Report the malaria status of this cell.
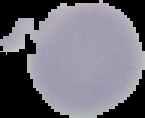

Uninfected.

Summary:
  - Image size: 145×118 pixels
  - Image type: segmented cell region with the area outside set to black
  - Preparation: thin blood film